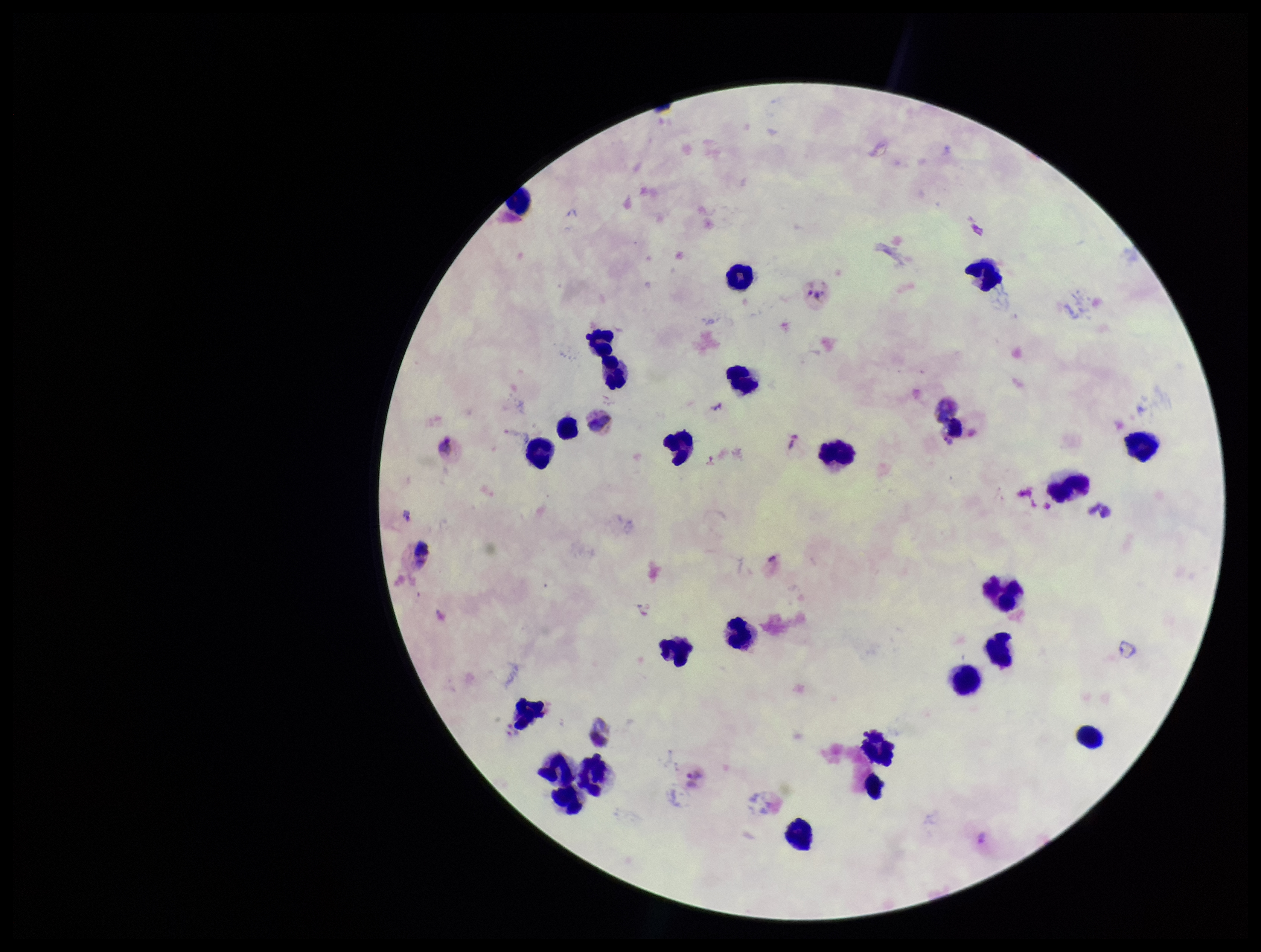
leukocyte_count: 25
field_of_view: single
preparation: thick blood smear
species_reported_for_this_patient: Plasmodium vivax
plasmodium_parasites: none identified
image_size: 1261×952 pixels
parasite_count: 0
stain: Giemsa
patient_malaria_status: infected
capture: smartphone photograph through the microscope eyepiece